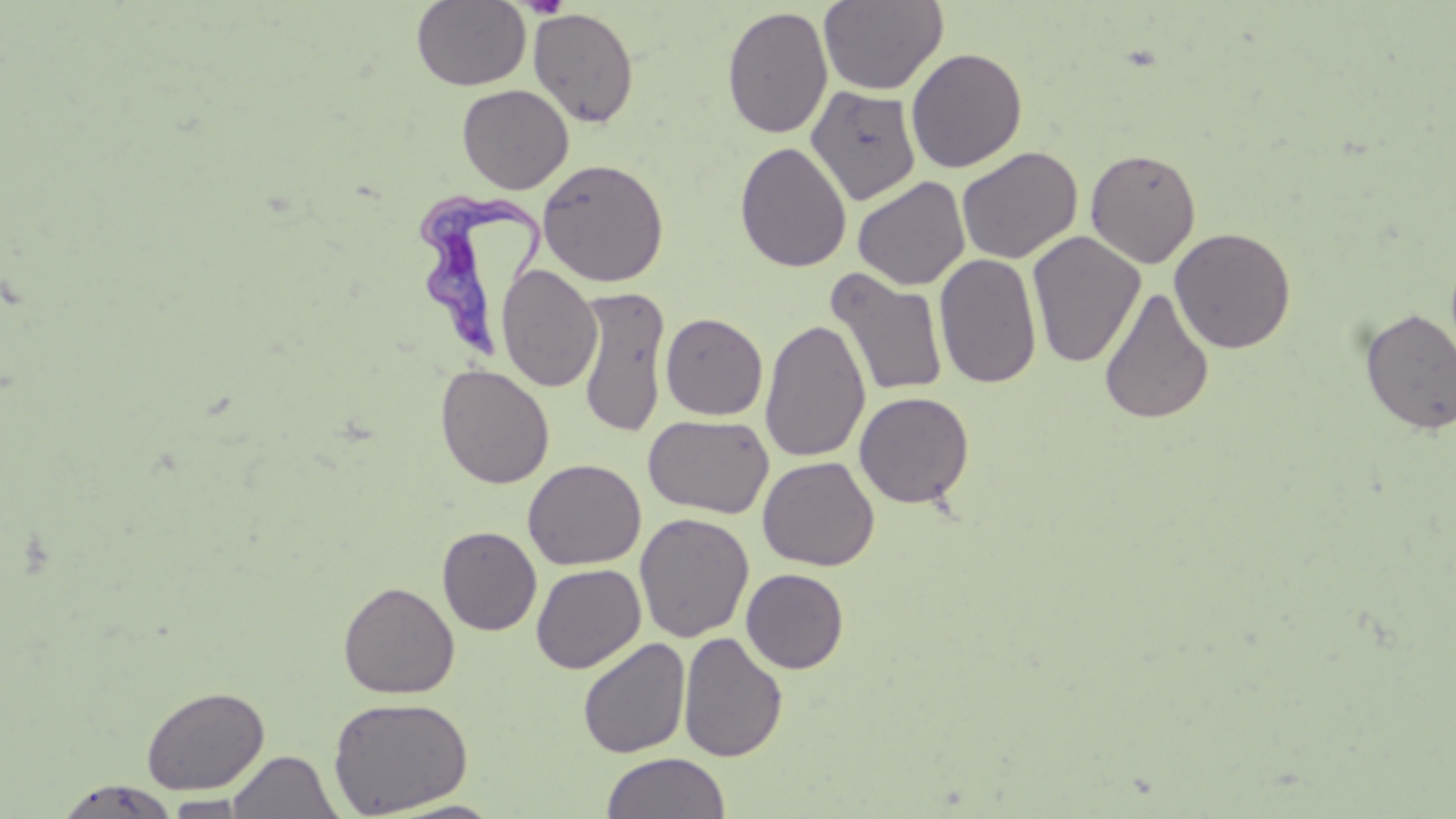
slide_level_diagnosis: Trypanosoma brucei
image_size: 1456×819 pixels
magnification: 1000x
platelet_locations: 'approximate bounding boxes as [x1, y1, x2, y2] in pixels: [523, 0, 569, 18]'
stain: May-Grünwald-Giemsa
preparation: thin blood smear
modality: optical microscopy
field_of_view: one of a larger specimen
trypanosoma_brucei_locations: 'approximate bounding boxes as [x1, y1, x2, y2] in pixels: [415, 179, 551, 362]'
uninfected_red_blood_cell_locations: 'approximate bounding boxes as [x1, y1, x2, y2] in pixels: [411, 0, 530, 91], [818, 0, 948, 95], [722, 5, 833, 139], [528, 7, 640, 128], [906, 47, 1028, 173], [457, 84, 574, 194], [806, 85, 921, 205], [735, 141, 852, 273], [956, 146, 1082, 264], [1085, 148, 1202, 268], [537, 158, 670, 287], [852, 176, 970, 291], [1169, 226, 1297, 353], [1027, 231, 1146, 368], [934, 252, 1042, 389], [496, 265, 602, 394], [826, 268, 949, 399], [574, 286, 670, 438], [1099, 286, 1215, 425], [1359, 307, 1456, 435], [660, 312, 768, 420], [760, 319, 870, 462], [436, 364, 554, 489], [853, 391, 975, 509], [643, 414, 773, 519], [757, 456, 879, 572], [523, 458, 646, 570], [634, 512, 754, 643], [437, 526, 541, 635], [531, 563, 646, 674], [741, 568, 849, 673], [338, 580, 460, 699], [678, 631, 788, 763], [577, 636, 690, 758], [141, 685, 269, 795], [328, 696, 474, 816], [226, 750, 342, 818], [601, 751, 731, 819], [52, 779, 182, 817], [163, 795, 254, 817], [375, 798, 512, 818]'